Outline each blood parasite and name the species.
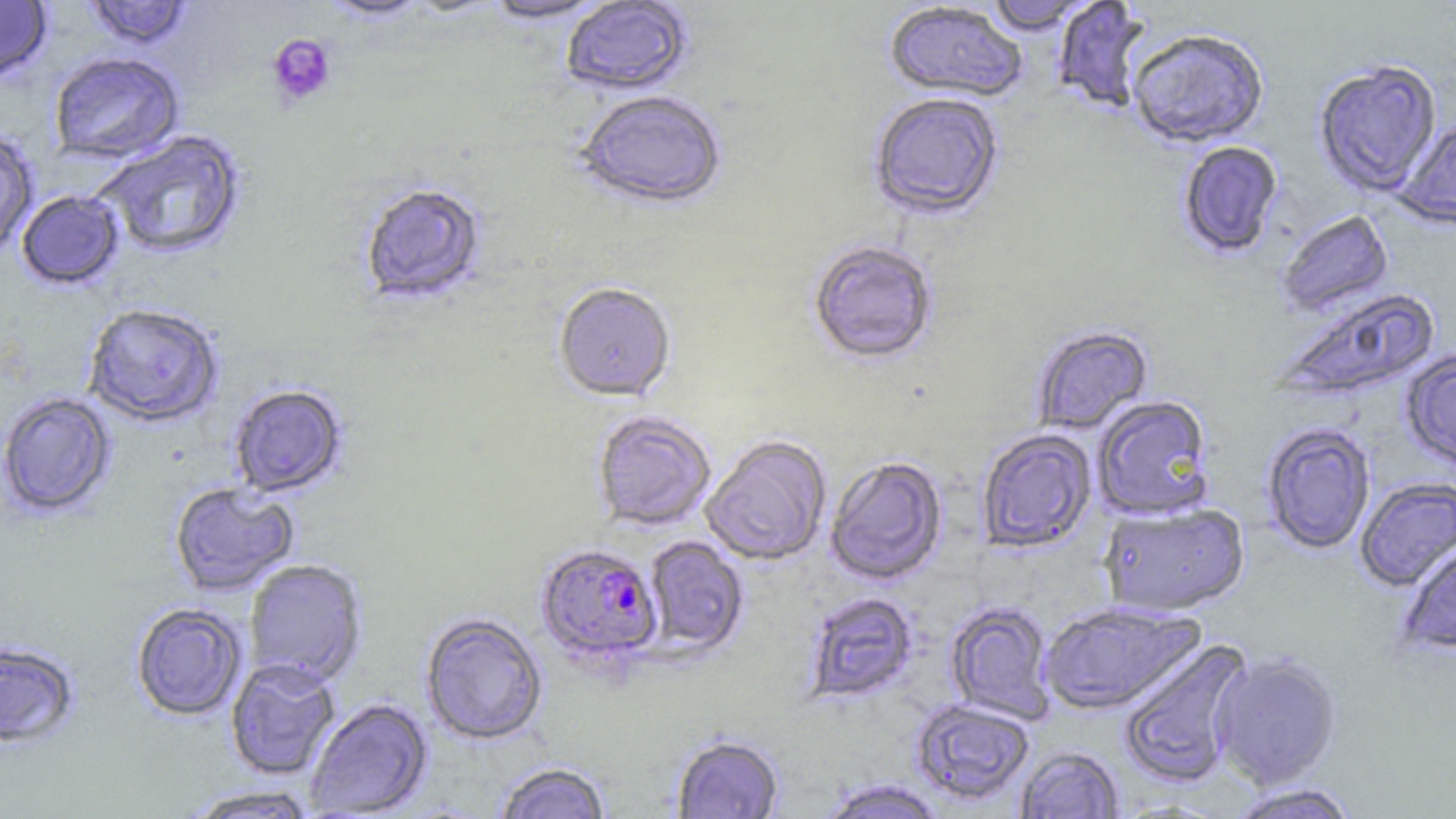

Approximate bounding boxes as [x1, y1, x2, y2] in pixels.
Plasmodium falciparum-infected red blood cells: [535, 543, 664, 666].
No Plasmodium ovale, Plasmodium malariae, Plasmodium vivax, Babesia divergens, or Trypanosoma brucei observed.

slide-level diagnosis = Plasmodium falciparum
stain = May-Grünwald-Giemsa
platelet locations = approximate bounding boxes as [x1, y1, x2, y2] in pixels: [266, 35, 337, 108]
uninfected red blood cell locations = approximate bounding boxes as [x1, y1, x2, y2] in pixels: [0, 0, 53, 84], [84, 0, 194, 50], [318, 0, 430, 22], [401, 0, 505, 18], [482, 0, 614, 25], [984, 0, 1096, 36], [560, 1, 694, 97], [1052, 1, 1153, 114], [883, 3, 1027, 103], [1128, 30, 1268, 150], [49, 52, 184, 165], [1314, 60, 1442, 197], [573, 92, 726, 212], [869, 94, 1004, 222], [1393, 119, 1455, 230], [0, 130, 39, 256], [96, 131, 246, 259], [1178, 142, 1283, 259], [360, 183, 487, 307], [16, 191, 124, 291], [1277, 210, 1394, 318], [808, 241, 938, 365], [554, 284, 676, 402], [1277, 286, 1440, 402], [83, 305, 223, 428], [1032, 326, 1153, 435], [1400, 350, 1456, 469], [229, 385, 347, 498], [1, 392, 117, 519], [1092, 396, 1215, 521], [592, 411, 717, 531], [1261, 423, 1376, 555], [976, 429, 1097, 554], [701, 435, 832, 566], [825, 456, 948, 586], [1355, 477, 1456, 591], [169, 483, 299, 596], [1099, 502, 1250, 618], [643, 536, 749, 658], [1395, 543, 1456, 655], [244, 560, 367, 687], [804, 592, 919, 705], [945, 601, 1056, 725], [1039, 601, 1205, 716], [131, 603, 247, 721], [420, 612, 548, 745], [1117, 638, 1253, 789], [0, 643, 80, 749], [1210, 652, 1342, 790], [226, 658, 341, 780], [304, 698, 433, 817], [911, 700, 1034, 806], [671, 734, 784, 818], [1014, 745, 1124, 818], [494, 761, 613, 819], [818, 779, 949, 819], [1225, 783, 1361, 819], [184, 786, 321, 818]
field of view = one of a larger specimen
magnification = 1000x
modality = light microscopy
image size = 1456×819 pixels
preparation = thin blood smear